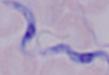
{
  "magnification": "1000x",
  "identification": "trypanosome",
  "modality": "photomicrograph"
}